Point out every malaria parasite and every leukocyte.
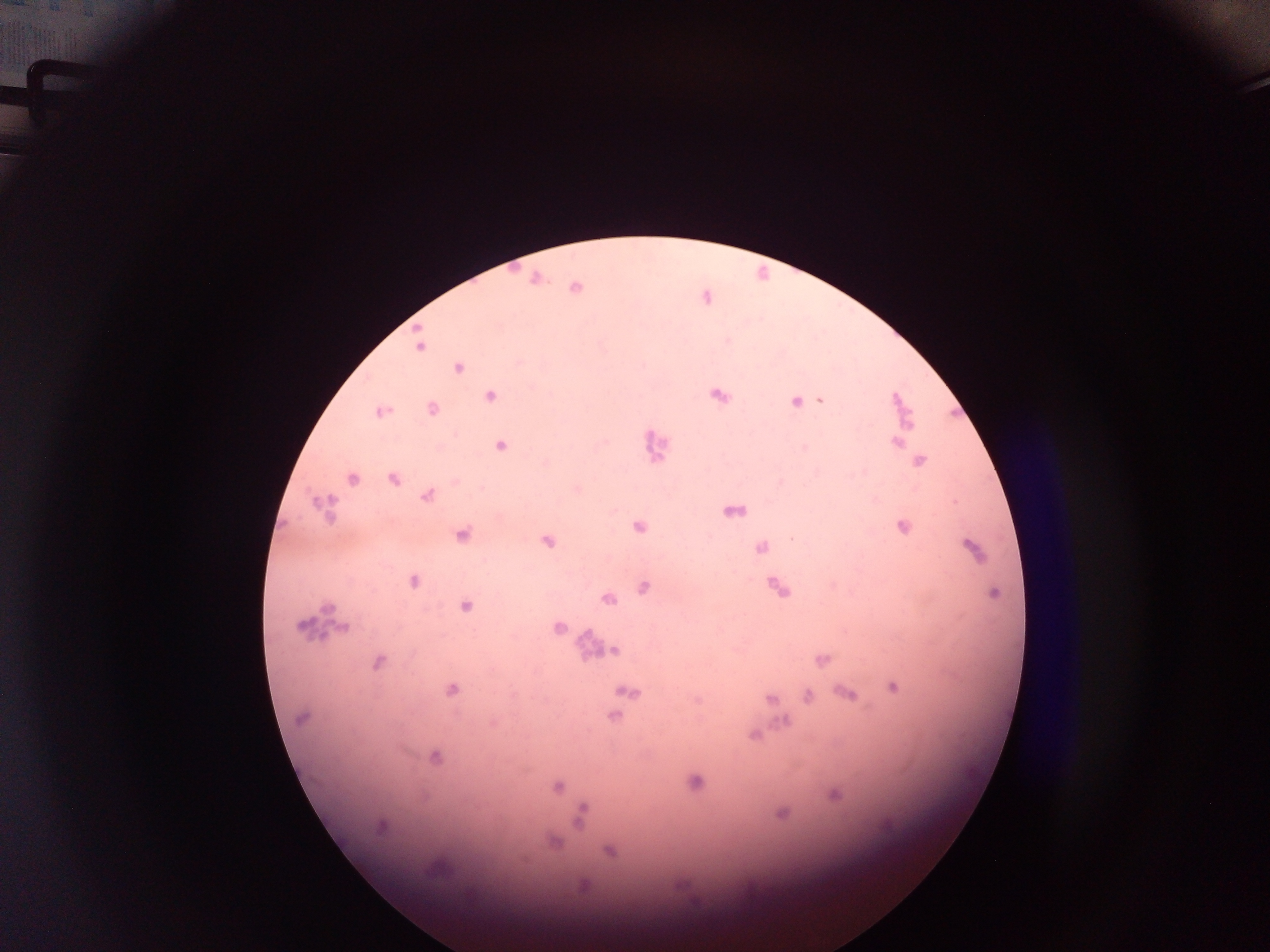
Approximate centers as x y in pixels.
Malaria parasites: 537 278; 576 288; 419 347; 459 368; 491 395; 896 400; 821 401; 795 402; 432 409; 380 411; 909 425; 897 443; 501 446; 920 461; 353 478; 393 479; 427 496; 323 506; 639 526; 903 527; 462 535; 547 541; 761 547; 972 548; 413 581; 644 587; 994 593; 607 599; 466 607; 301 627; 557 627; 343 628; 615 651; 823 659; 378 662; 893 688; 451 690; 629 692; 848 693; 807 695; 770 699; 774 708; 615 716; 301 718; 784 721; 753 735; 435 756; 695 781; 557 787; 834 795; 781 814; 580 815; 380 827; 553 842; 609 850; 583 885.
Leukocytes: 655 445; 583 643.

{
  "field_of_view": "single",
  "image_size": "1270×952 pixels",
  "capture": "mobile-phone photograph through a microscope",
  "preparation": "thick blood smear",
  "country": "Ghana"
}